Assess for malaria.
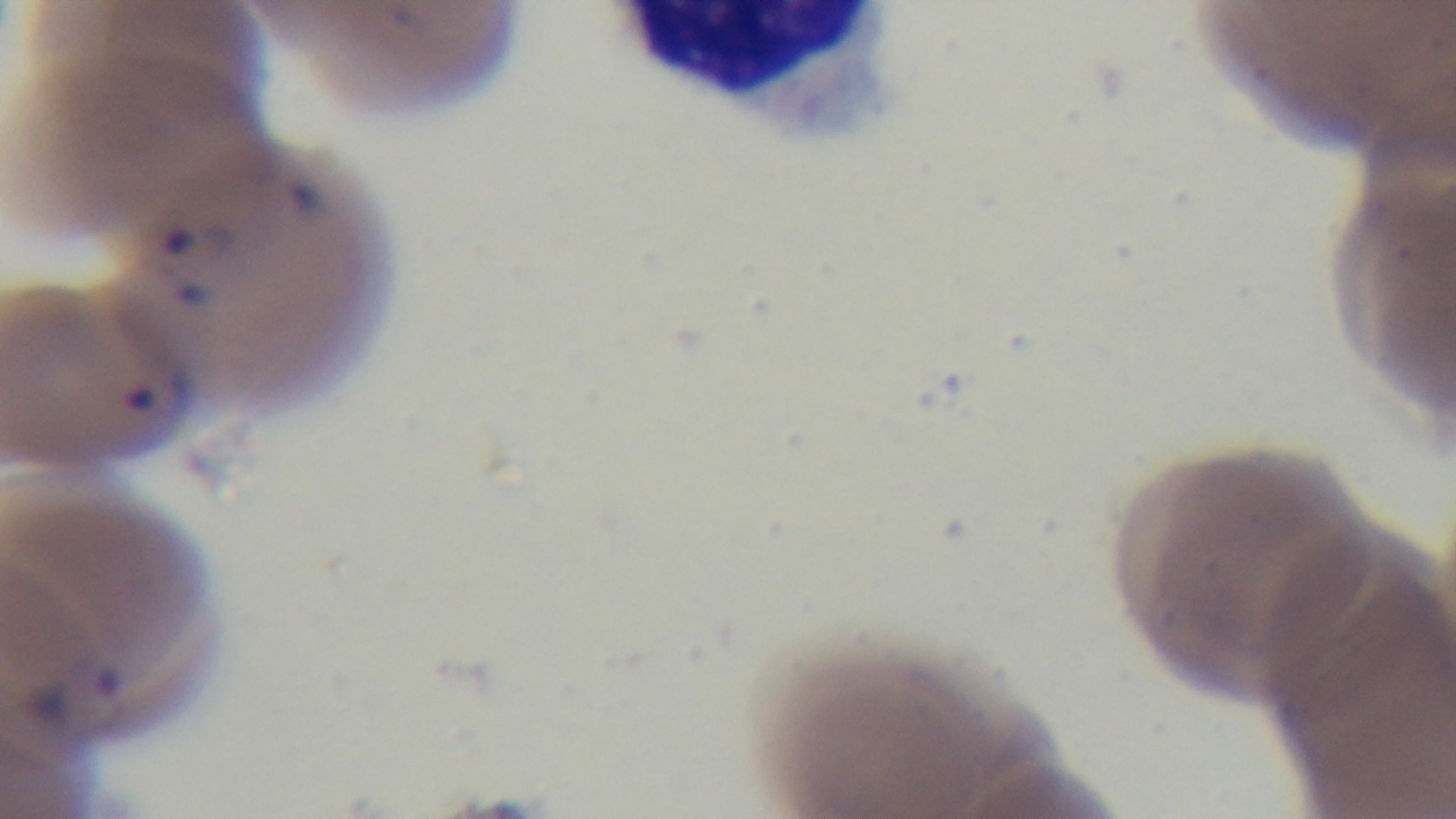

It is infected.

Captured with a mounted 4K digital camera. Photomicrograph. Giemsa stain. Preparation: thin. Oil-immersion objective, 100x. Single field of view.